Name the parasite shown.
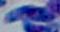
This is Toxoplasma gondii.

Summary:
  - Modality: micrograph
  - Magnification: 1000x